Point out every Plasmodium parasite and every leukocyte.
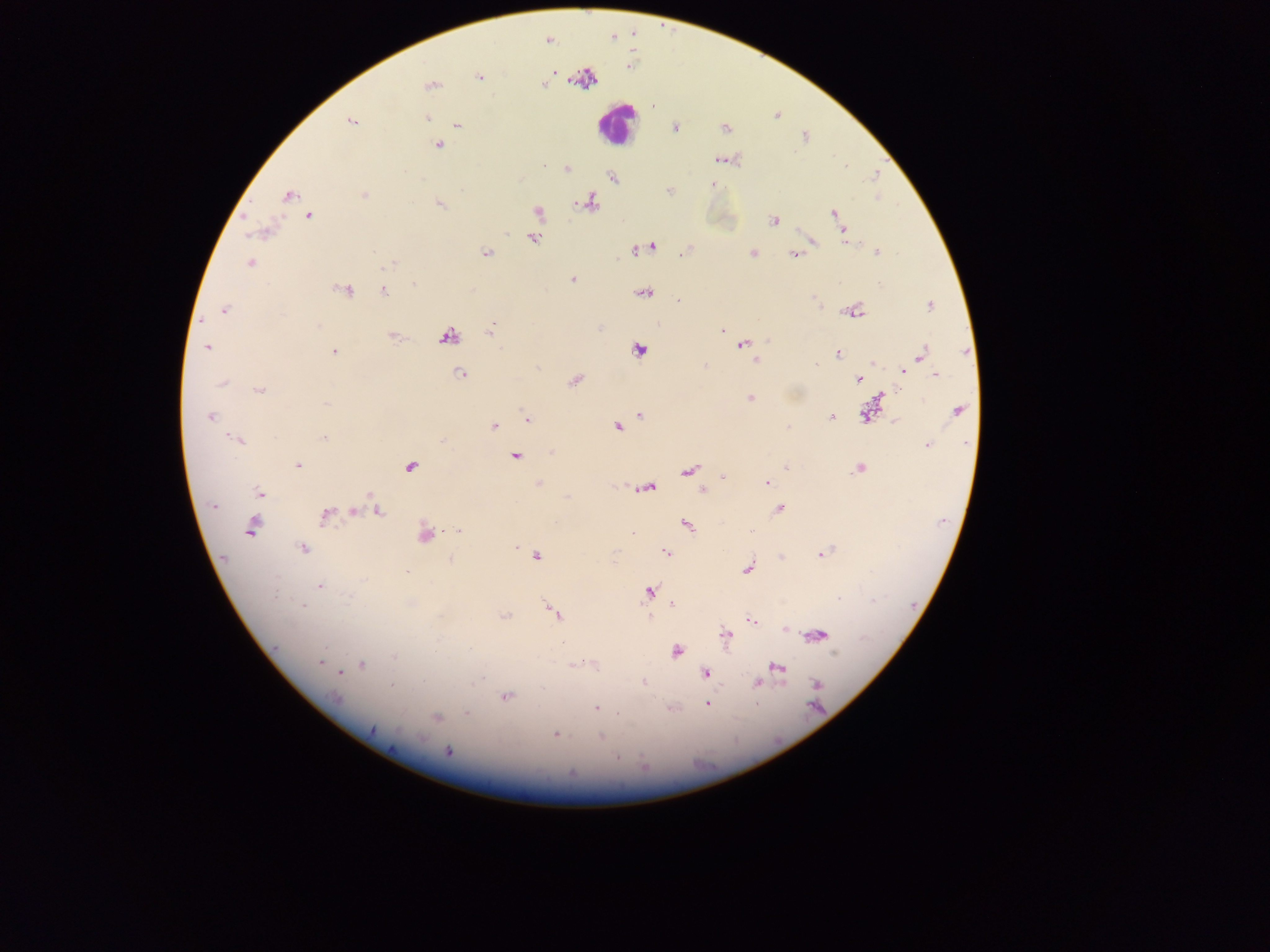
Approximate centers as {x, y} in pixels.
Plasmodium parasites (some below the resolvable threshold): {549, 40}, {553, 72}, {584, 76}, {479, 77}, {544, 85}, {430, 86}, {427, 118}, {351, 120}, {457, 125}, {675, 129}, {725, 129}, {805, 137}, {439, 145}, {718, 159}, {567, 169}, {613, 177}, {713, 185}, {669, 191}, {364, 195}, {288, 196}, {590, 202}, {440, 204}, {538, 211}, {834, 213}, {309, 215}, {774, 221}, {844, 232}, {533, 238}, {813, 242}, {652, 247}, {636, 250}, {685, 252}, {877, 252}, {753, 253}, {487, 254}, {793, 255}, {250, 262}, {391, 263}, {572, 279}, {413, 283}, {879, 284}, {344, 289}, {385, 291}, {645, 292}, {679, 300}, {929, 305}, {224, 310}, {855, 312}, {319, 325}, {491, 331}, {722, 331}, {392, 336}, {447, 336}, {768, 340}, {742, 345}, {206, 347}, {638, 350}, {335, 351}, {920, 353}, {838, 354}, {757, 361}, {873, 363}, {815, 365}, {704, 366}, {903, 371}, {936, 373}, {459, 374}, {859, 379}, {575, 380}, {223, 382}, {260, 389}, {881, 396}, {750, 397}, {326, 404}, {958, 411}, {866, 414}, {640, 415}, {210, 416}, {831, 417}, {526, 418}, {895, 421}, {494, 426}, {617, 427}, {787, 427}, {325, 437}, {238, 440}, {927, 445}, {551, 452}, {515, 456}, {298, 465}, {411, 466}, {786, 467}, {858, 468}, {689, 470}, {724, 476}, {539, 483}, {766, 483}, {649, 487}, {702, 490}, {260, 493}, {214, 506}, {778, 509}, {354, 512}, {378, 512}, {325, 516}, {687, 526}, {252, 527}, {458, 530}, {633, 532}, {425, 535}, {515, 548}, {303, 549}, {665, 553}, {822, 554}, {538, 556}, {781, 557}, {451, 560}, {748, 569}, {406, 572}, {320, 586}, {649, 591}, {349, 598}, {673, 604}, {303, 606}, {554, 612}, {505, 616}, {750, 620}, {786, 629}, {818, 635}, {726, 636}, {436, 650}, {676, 652}, {834, 653}, {394, 657}, {320, 662}, {362, 665}, {571, 665}, {778, 667}, {339, 672}, {705, 673}, {643, 682}, {757, 683}, {817, 684}, {390, 685}, {336, 697}, {506, 697}, {707, 704}, {596, 707}, {671, 708}, {617, 712}, {467, 713}, {437, 717}, {372, 730}, {555, 734}, {601, 737}, {448, 751}, {617, 757}.
Leukocytes: {615, 124}.

Sample from Ghana. Thick blood smear. One field of view. Photographed through a microscope with a mobile-phone camera. Image is 1270×952 pixels.